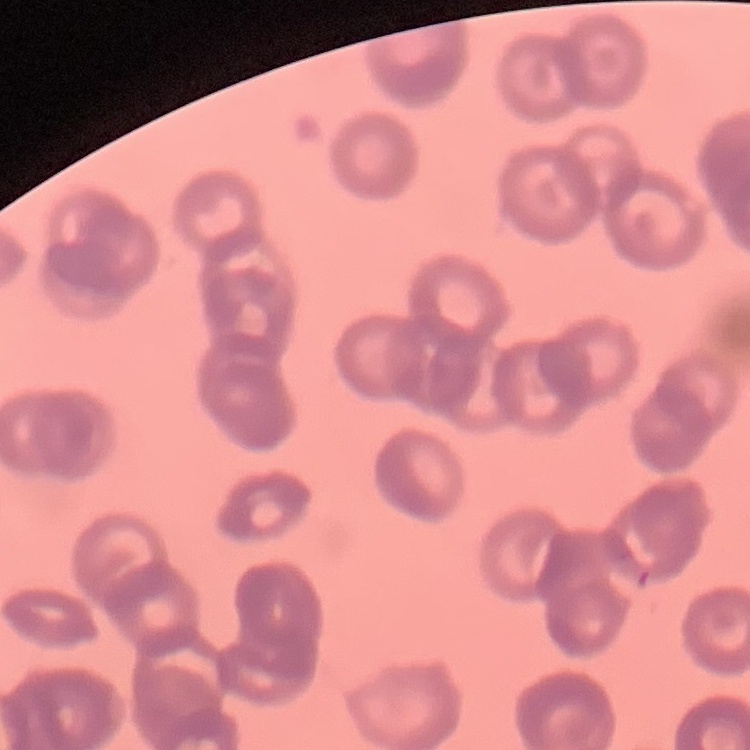
Summary:
  - Erythrocyte morphology: rouleaux formation
  - Image type: square crop of a larger photomicrograph
  - Preparation: thin blood smear
  - Stain: Field's or Giemsa